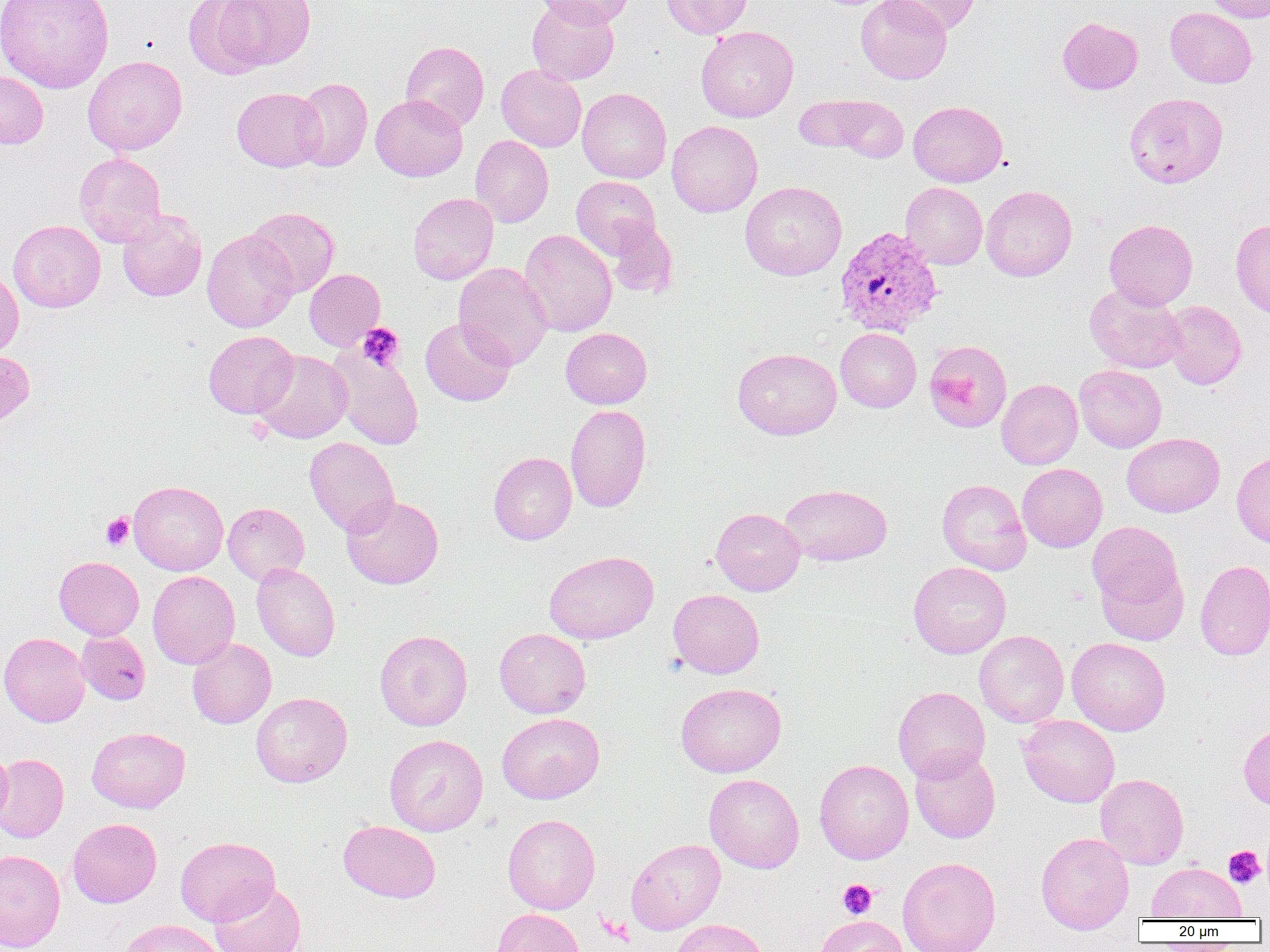

Summary:
  - Coordinate format: approximate bounding boxes as named x1/y1/x2/y2 corners in pixels
  - Uninfected red blood cell locations: (x1=1, y1=0, x2=114, y2=93), (x1=184, y1=0, x2=272, y2=78), (x1=527, y1=0, x2=619, y2=85), (x1=535, y1=0, x2=634, y2=28), (x1=662, y1=0, x2=753, y2=39), (x1=856, y1=0, x2=952, y2=84), (x1=883, y1=0, x2=981, y2=36), (x1=1203, y1=0, x2=1270, y2=23), (x1=212, y1=1, x2=316, y2=71), (x1=1165, y1=7, x2=1257, y2=88), (x1=1057, y1=17, x2=1143, y2=95), (x1=696, y1=25, x2=799, y2=123), (x1=400, y1=40, x2=489, y2=131), (x1=83, y1=55, x2=187, y2=155), (x1=496, y1=64, x2=586, y2=152), (x1=0, y1=71, x2=48, y2=148), (x1=293, y1=78, x2=373, y2=172), (x1=232, y1=87, x2=326, y2=171), (x1=577, y1=88, x2=672, y2=183), (x1=1124, y1=92, x2=1228, y2=188), (x1=371, y1=94, x2=467, y2=181), (x1=796, y1=96, x2=870, y2=152), (x1=831, y1=96, x2=908, y2=163), (x1=908, y1=100, x2=1008, y2=187), (x1=666, y1=120, x2=763, y2=217), (x1=470, y1=135, x2=553, y2=228), (x1=74, y1=152, x2=167, y2=247), (x1=571, y1=175, x2=660, y2=258), (x1=740, y1=181, x2=847, y2=280), (x1=900, y1=182, x2=987, y2=269), (x1=981, y1=185, x2=1077, y2=281), (x1=408, y1=193, x2=498, y2=285), (x1=246, y1=207, x2=339, y2=297), (x1=117, y1=210, x2=207, y2=301), (x1=1230, y1=218, x2=1270, y2=318), (x1=8, y1=219, x2=106, y2=312), (x1=1104, y1=219, x2=1198, y2=309), (x1=606, y1=222, x2=677, y2=298), (x1=202, y1=229, x2=298, y2=333), (x1=519, y1=229, x2=617, y2=337), (x1=453, y1=262, x2=553, y2=368), (x1=304, y1=269, x2=386, y2=351), (x1=0, y1=270, x2=24, y2=358), (x1=1085, y1=283, x2=1185, y2=374), (x1=1163, y1=300, x2=1247, y2=390), (x1=420, y1=317, x2=516, y2=406), (x1=561, y1=327, x2=652, y2=409), (x1=835, y1=328, x2=921, y2=412), (x1=203, y1=330, x2=299, y2=418), (x1=923, y1=339, x2=1012, y2=433), (x1=328, y1=345, x2=425, y2=450), (x1=733, y1=347, x2=842, y2=440), (x1=253, y1=349, x2=353, y2=444), (x1=0, y1=350, x2=34, y2=428), (x1=1074, y1=364, x2=1167, y2=453), (x1=996, y1=378, x2=1083, y2=469), (x1=565, y1=403, x2=651, y2=513), (x1=1122, y1=432, x2=1225, y2=517), (x1=304, y1=437, x2=400, y2=537), (x1=1231, y1=451, x2=1270, y2=549), (x1=488, y1=452, x2=577, y2=545), (x1=1017, y1=463, x2=1107, y2=552), (x1=936, y1=478, x2=1032, y2=575), (x1=128, y1=480, x2=228, y2=575), (x1=780, y1=484, x2=892, y2=566), (x1=342, y1=495, x2=444, y2=589), (x1=223, y1=502, x2=310, y2=585), (x1=711, y1=507, x2=805, y2=596), (x1=1088, y1=519, x2=1186, y2=620), (x1=544, y1=550, x2=659, y2=644), (x1=54, y1=556, x2=144, y2=640), (x1=1195, y1=559, x2=1270, y2=660), (x1=908, y1=561, x2=1011, y2=659), (x1=252, y1=562, x2=340, y2=662), (x1=148, y1=570, x2=239, y2=669), (x1=668, y1=589, x2=764, y2=678), (x1=494, y1=628, x2=591, y2=718), (x1=76, y1=630, x2=150, y2=705), (x1=374, y1=630, x2=473, y2=730), (x1=974, y1=630, x2=1069, y2=728), (x1=0, y1=632, x2=90, y2=727), (x1=187, y1=637, x2=276, y2=729), (x1=1067, y1=637, x2=1170, y2=735), (x1=676, y1=683, x2=786, y2=777), (x1=893, y1=686, x2=990, y2=782), (x1=250, y1=692, x2=352, y2=787), (x1=497, y1=712, x2=604, y2=803), (x1=1018, y1=715, x2=1119, y2=807), (x1=1238, y1=721, x2=1270, y2=810), (x1=86, y1=727, x2=190, y2=813), (x1=384, y1=734, x2=488, y2=836), (x1=0, y1=744, x2=12, y2=831), (x1=909, y1=748, x2=1000, y2=843), (x1=0, y1=753, x2=69, y2=842), (x1=815, y1=759, x2=914, y2=864), (x1=1095, y1=773, x2=1189, y2=869), (x1=704, y1=774, x2=804, y2=873), (x1=503, y1=813, x2=600, y2=914), (x1=67, y1=818, x2=162, y2=908), (x1=338, y1=820, x2=441, y2=903), (x1=1035, y1=832, x2=1135, y2=933), (x1=175, y1=836, x2=280, y2=926), (x1=626, y1=838, x2=726, y2=934), (x1=0, y1=849, x2=65, y2=951), (x1=897, y1=857, x2=1001, y2=952), (x1=1146, y1=861, x2=1247, y2=921), (x1=209, y1=881, x2=307, y2=952), (x1=492, y1=908, x2=585, y2=952), (x1=813, y1=915, x2=910, y2=952), (x1=120, y1=919, x2=225, y2=952), (x1=669, y1=919, x2=769, y2=952)
  - Plasmodium vivax-infected red blood cell locations: (x1=835, y1=226, x2=944, y2=338)
  - Platelet locations: (x1=357, y1=322, x2=404, y2=370), (x1=246, y1=418, x2=273, y2=444), (x1=100, y1=512, x2=134, y2=550), (x1=1223, y1=846, x2=1265, y2=887), (x1=838, y1=879, x2=878, y2=918)
  - Slide-level diagnosis: Plasmodium vivax
  - Field of view: one of a larger specimen
  - Preparation: thin blood film
  - Modality: light microscopy
  - Magnification: 1000x
  - Image size: 1270×952 pixels